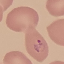

Summary:
  - Malaria status: parasitized
  - Capture: smartphone camera at the microscope eyepiece
  - Preparation: thin smear
  - Stain: Giemsa
  - Image type: automatically extracted cell patch, resized to 64 × 64 pixels